Name the parasite shown.
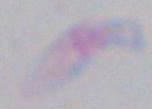
This is Toxoplasma gondii.

Summary:
  - Modality: photomicrograph
  - Magnification: 1000x